Give the extent of all Plasmodium vivax-infected red blood cells.
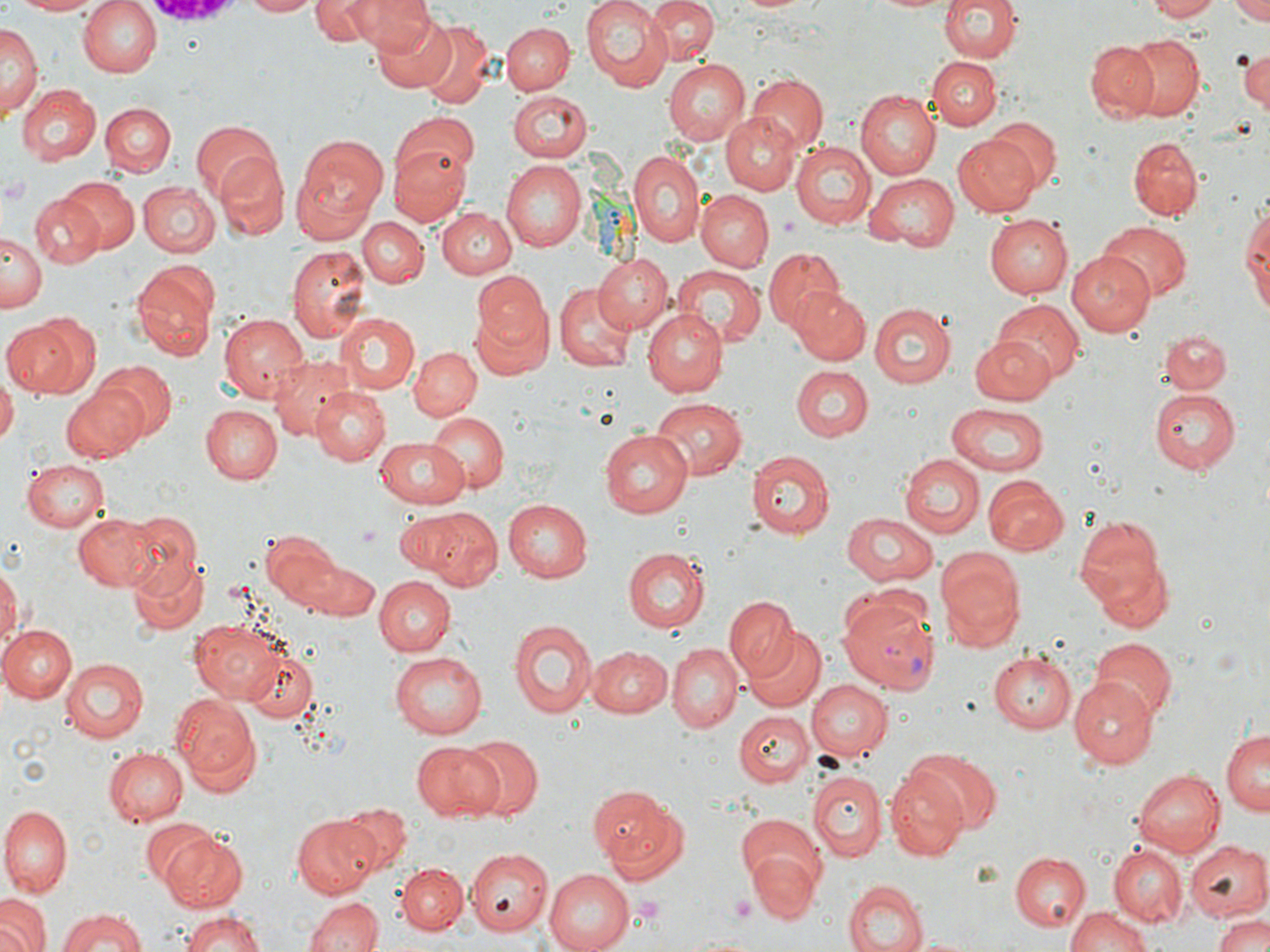
Approximate bounding boxes as [x1, y1, x2, y2] in pixels.
Plasmodium vivax-infected red blood cells: [839, 590, 940, 695].

slide-level diagnosis = Plasmodium vivax
uninfected red blood cell locations = approximate bounding boxes as [x1, y1, x2, y2] in pixels: [4, 0, 111, 16], [77, 0, 162, 77], [240, 0, 321, 16], [311, 0, 378, 45], [352, 0, 443, 65], [578, 0, 673, 90], [646, 0, 718, 64], [734, 0, 816, 16], [863, 0, 959, 15], [939, 0, 1020, 64], [1143, 0, 1222, 21], [1230, 1, 1270, 25], [372, 13, 455, 91], [418, 21, 494, 108], [502, 22, 574, 94], [3, 25, 39, 116], [1124, 33, 1205, 119], [1086, 42, 1159, 122], [1234, 46, 1270, 113], [928, 57, 1001, 130], [662, 58, 751, 147], [748, 74, 827, 151], [15, 83, 99, 165], [508, 89, 593, 163], [855, 91, 939, 181], [99, 101, 175, 176], [721, 111, 804, 195], [391, 114, 481, 195], [981, 119, 1059, 194], [190, 122, 279, 207], [951, 135, 1039, 216], [1127, 136, 1203, 222], [294, 137, 389, 234], [791, 141, 874, 231], [389, 145, 470, 225], [628, 148, 706, 247], [214, 151, 290, 238], [502, 163, 586, 250], [866, 173, 961, 248], [59, 176, 138, 254], [137, 181, 220, 258], [697, 190, 773, 270], [31, 193, 105, 268], [1239, 203, 1269, 321], [440, 206, 518, 278], [985, 214, 1072, 299], [359, 217, 427, 288], [1097, 222, 1190, 301], [2, 231, 44, 310], [288, 245, 371, 346], [763, 246, 844, 332], [1067, 250, 1155, 334], [592, 253, 672, 334], [133, 261, 219, 361], [673, 267, 764, 349], [472, 271, 553, 352], [554, 281, 635, 373], [790, 285, 871, 365], [994, 300, 1084, 384], [470, 301, 554, 382], [870, 304, 957, 388], [335, 311, 417, 393], [643, 311, 729, 397], [6, 312, 99, 398], [218, 312, 308, 401], [1159, 328, 1230, 395], [970, 337, 1056, 403], [409, 347, 481, 422], [269, 356, 354, 441], [94, 362, 177, 441], [790, 366, 873, 439], [0, 378, 17, 442], [60, 384, 148, 464], [313, 387, 390, 465], [1150, 390, 1242, 475], [649, 398, 747, 479], [947, 402, 1051, 475], [200, 405, 282, 484], [426, 412, 509, 494], [598, 430, 692, 518], [374, 435, 468, 506], [746, 451, 834, 540], [899, 455, 983, 538], [24, 458, 110, 532], [982, 477, 1066, 554], [502, 499, 593, 582], [411, 507, 500, 588], [74, 512, 156, 590], [121, 512, 203, 594], [839, 512, 937, 588], [1073, 518, 1165, 615], [262, 530, 346, 608], [624, 548, 708, 632], [935, 551, 1023, 649], [128, 555, 207, 634], [1091, 555, 1174, 635], [302, 560, 380, 621], [0, 563, 20, 653], [375, 576, 455, 656], [725, 597, 798, 680], [190, 618, 286, 702], [509, 619, 597, 719], [0, 623, 77, 702], [744, 626, 827, 713], [1092, 639, 1176, 723], [666, 644, 741, 733], [241, 645, 319, 724], [585, 646, 670, 719], [992, 649, 1077, 732], [387, 652, 487, 739], [59, 656, 149, 742], [1072, 675, 1160, 765], [806, 679, 891, 760], [172, 693, 259, 789], [734, 710, 813, 787], [1221, 729, 1270, 817], [456, 735, 543, 820], [410, 739, 505, 821], [103, 747, 187, 826], [913, 751, 1000, 831], [886, 767, 970, 861], [1132, 768, 1225, 859], [808, 769, 886, 861], [588, 785, 672, 863], [336, 801, 412, 870], [599, 804, 690, 886], [2, 805, 75, 897], [291, 815, 380, 896], [738, 815, 827, 893], [141, 817, 223, 889], [158, 829, 248, 911], [1184, 841, 1269, 920], [1109, 845, 1187, 926], [467, 849, 551, 936], [749, 851, 820, 924], [1010, 852, 1089, 930], [395, 862, 467, 933], [545, 868, 639, 952], [844, 878, 926, 952], [302, 894, 383, 952], [0, 895, 51, 952], [1064, 904, 1154, 951], [54, 908, 151, 950], [178, 908, 266, 952], [1212, 913, 1270, 952]
image size = 1270×952 pixels
preparation = thin blood smear
field of view = single
platelet locations = approximate bounding boxes as [x1, y1, x2, y2] in pixels: [0, 174, 36, 207], [357, 526, 380, 548], [727, 895, 757, 920], [629, 898, 665, 925]
stain = May-Grünwald-Giemsa
modality = optical microscopy
magnification = 1000x